Assess the morphology of the red blood cells.
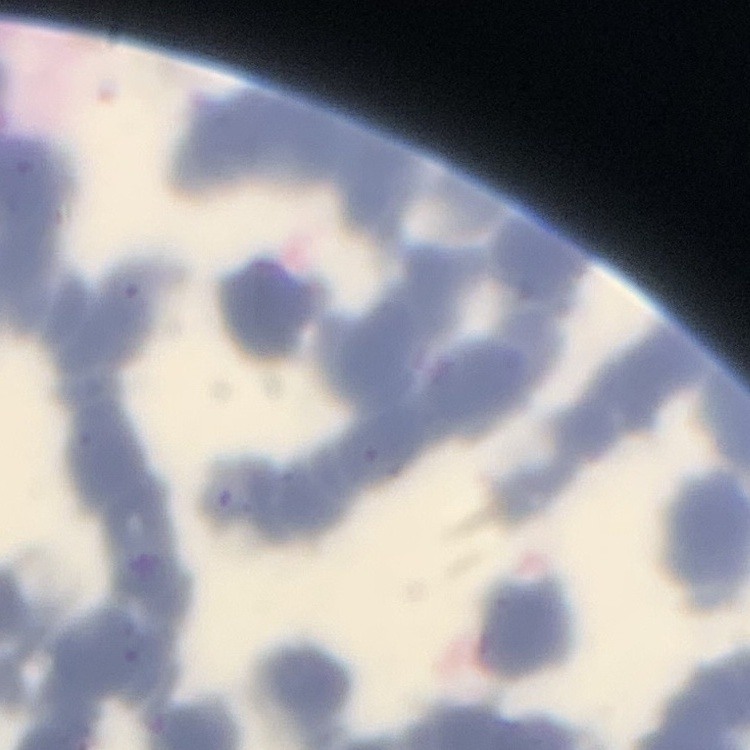

They show rouleaux formation.

preparation = thin blood smear
stain = Field's or Giemsa
image type = square crop of a larger photomicrograph